Name the cell type shown.
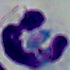

This is a leukocyte.

Summary:
  - Modality: photomicrograph
  - Magnification: 1000x